Name the parasite shown.
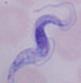
This is a trypanosome.

magnification = 1000x
modality = photomicrograph